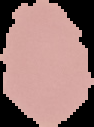

Summary:
  - Result: no Plasmodium parasites detected
  - Preparation: thin blood film
  - Image size: 94×127 pixels
  - Image type: segmented cell region on a black background